Classify this cell by malaria status.
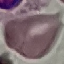

Uninfected.

Automatically extracted cell patch, resized to 64 × 64 pixels. Giemsa-stained preparation. Thin blood smear. Acquired by smartphone through the microscope eyepiece.